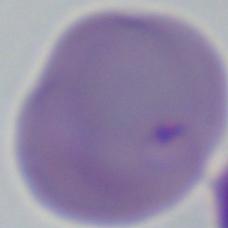
magnification: 1000x
identification: Babesia
modality: photomicrograph